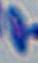
Summary:
  - Magnification: 1000x
  - Identification: Toxoplasma gondii
  - Modality: photomicrograph